Give the position of every leukocyte visible.
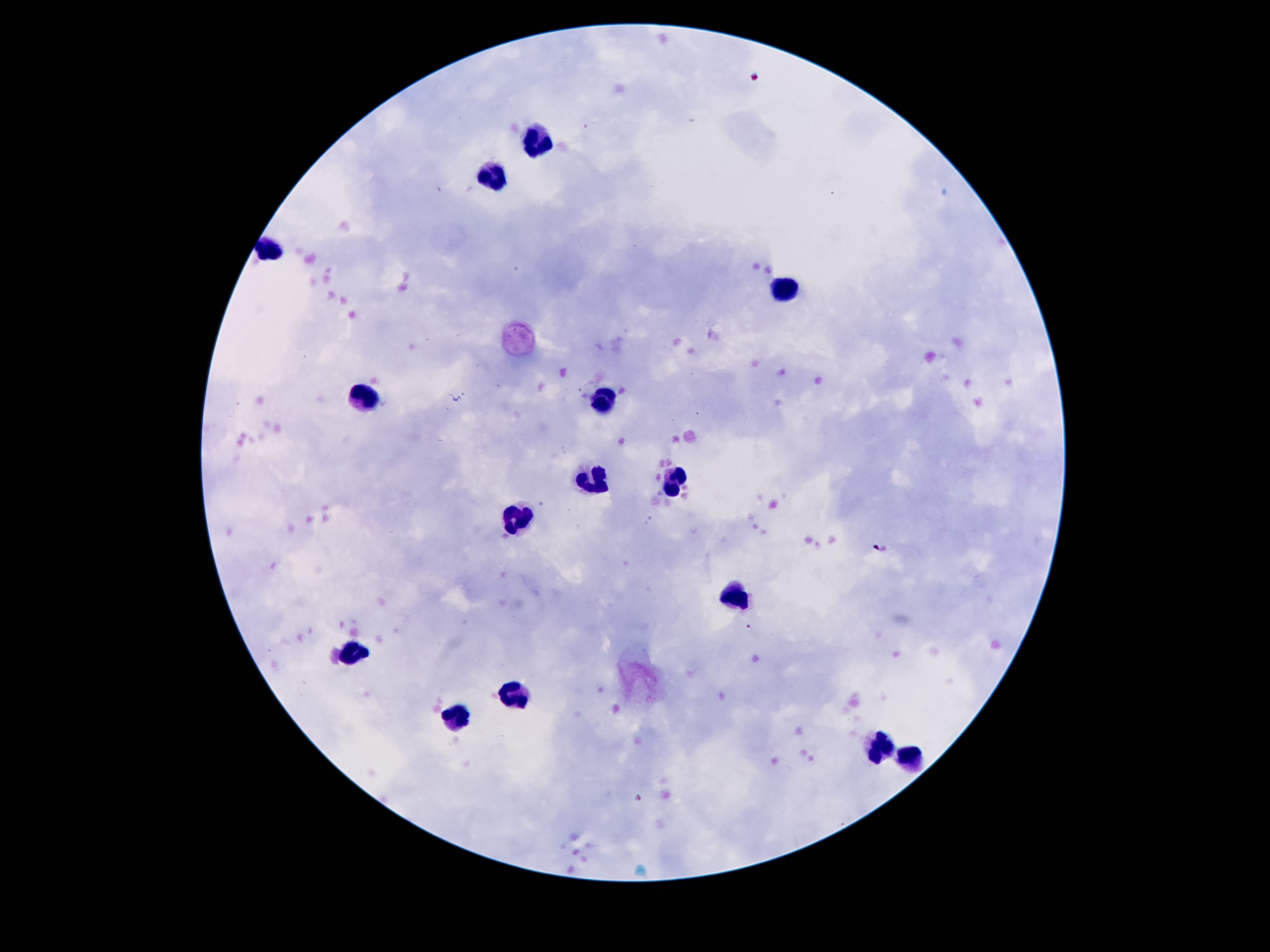

Approximate centers as [x, y] in pixels.
Leukocytes: [535, 137], [497, 174], [271, 249], [789, 288], [364, 400], [602, 403], [595, 480], [675, 480], [518, 523], [735, 591], [355, 651], [518, 697], [455, 719], [882, 749], [913, 758].

patient malaria status = not infected
stain = Giemsa
image size = 1270×952 pixels
field of view = one from this slide
capture = smartphone camera through the microscope eyepiece
preparation = thick blood smear
magnification = 100x